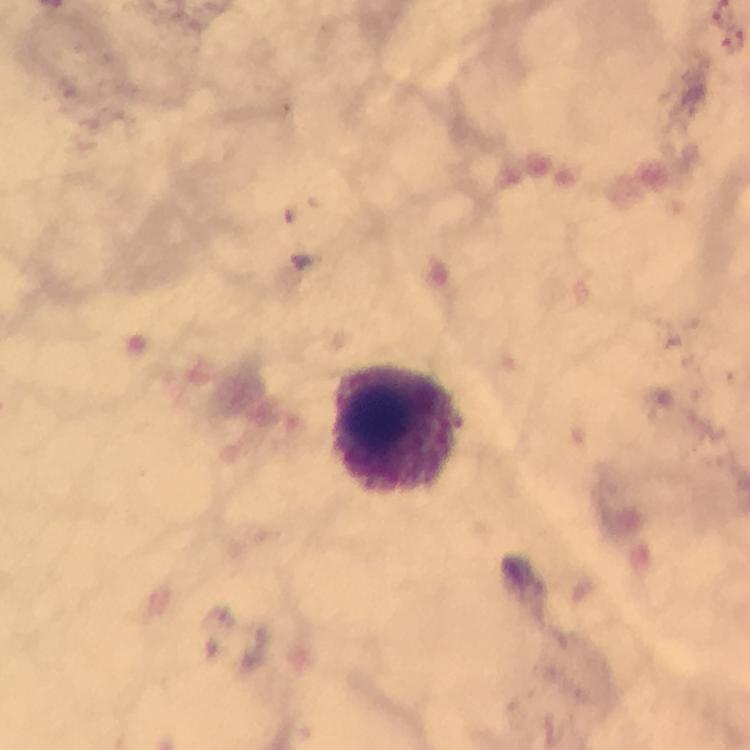

Approximate centers as (x, y) in pixels. Malaria parasite locations: (733, 41). Leukocyte locations: (400, 429). A crop from one field of view. Immersion oil applied. Photographed through the microscope with a smartphone camera. Giemsa stain. Thick blood film. Image is 750×750 pixels. From a malaria diagnostic workup. At 100x magnification.